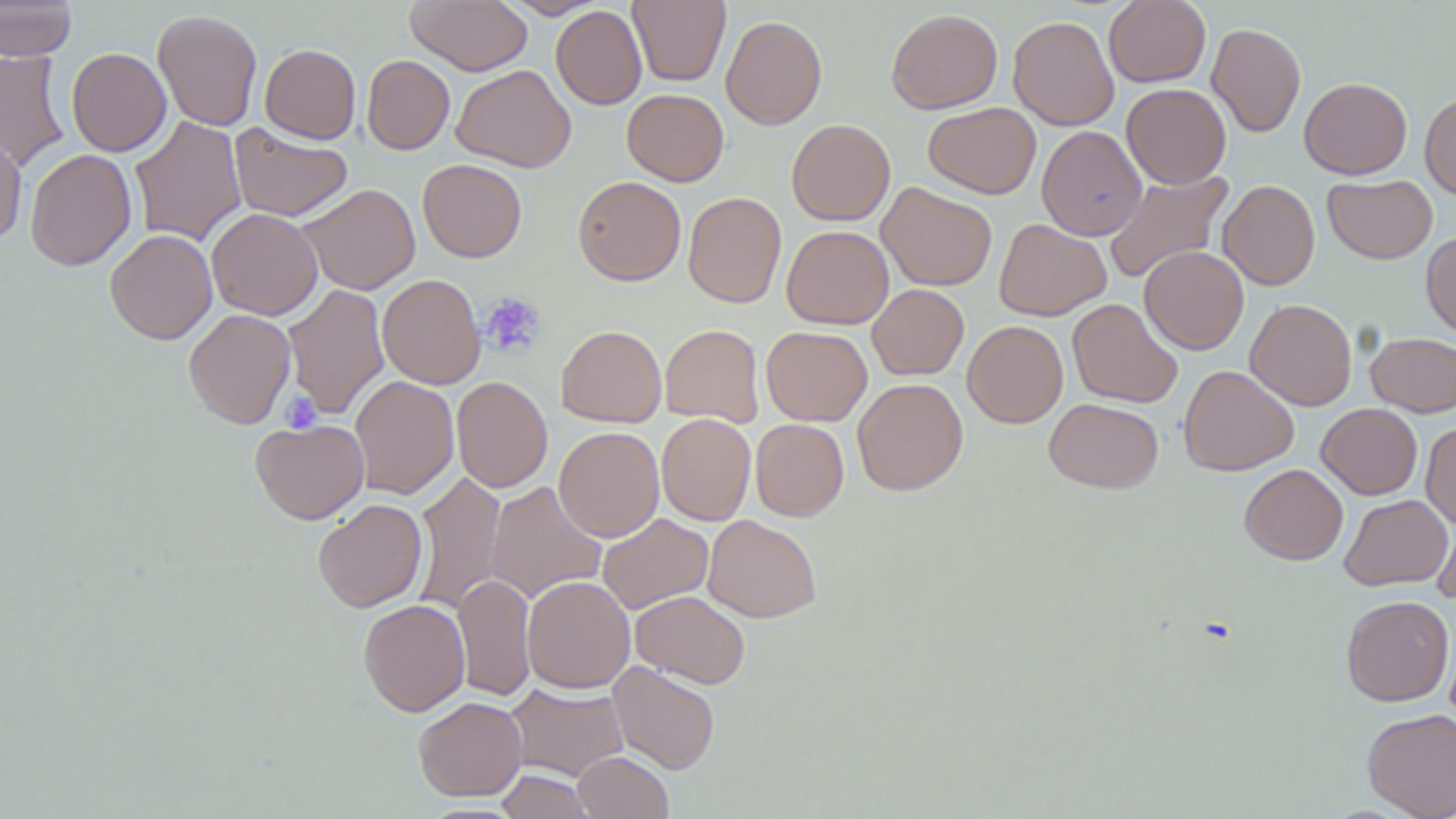
Summary:
  - Coordinate format: approximate bounding boxes as (x1, y1, x2, y2) in pixels
  - Platelet locations: (480, 292, 546, 357), (280, 391, 322, 432)
  - Uninfected red blood cell locations: (0, 0, 78, 61), (406, 0, 533, 75), (500, 0, 607, 19), (628, 0, 730, 86), (1104, 0, 1211, 87), (551, 6, 647, 110), (886, 8, 1003, 114), (152, 9, 263, 131), (721, 14, 827, 130), (1008, 15, 1119, 131), (1207, 23, 1306, 137), (260, 43, 361, 143), (66, 48, 171, 156), (0, 49, 69, 172), (362, 55, 455, 154), (451, 64, 576, 172), (1299, 77, 1412, 179), (1121, 83, 1231, 189), (622, 88, 729, 186), (1419, 92, 1456, 199), (923, 102, 1041, 199), (129, 116, 248, 247), (787, 119, 895, 225), (229, 124, 353, 222), (1036, 125, 1147, 241), (0, 132, 27, 247), (25, 149, 137, 271), (418, 158, 527, 262), (1102, 170, 1234, 286), (1322, 174, 1437, 264), (573, 176, 686, 286), (1218, 180, 1320, 290), (877, 182, 997, 291), (298, 183, 420, 295), (683, 191, 786, 308), (207, 208, 322, 320), (994, 218, 1111, 321), (781, 225, 894, 329), (105, 229, 217, 344), (1421, 231, 1456, 341), (1139, 246, 1249, 355), (377, 274, 485, 389), (283, 283, 390, 420), (867, 284, 969, 380), (1067, 298, 1183, 408), (1245, 298, 1357, 410), (184, 308, 296, 428), (962, 320, 1068, 428), (556, 324, 667, 427), (660, 324, 764, 428), (761, 326, 872, 426), (1365, 332, 1456, 416), (1178, 365, 1299, 476), (350, 375, 459, 500), (452, 376, 552, 492), (852, 378, 968, 495), (1044, 397, 1163, 493), (1317, 403, 1422, 500), (657, 413, 755, 525), (751, 418, 849, 521), (251, 419, 369, 524), (1420, 422, 1456, 529), (554, 426, 664, 542), (1239, 463, 1348, 565), (412, 470, 507, 614), (484, 481, 606, 603), (1339, 494, 1452, 591), (313, 498, 428, 612), (1432, 508, 1456, 603), (597, 513, 713, 614), (702, 515, 821, 622), (453, 574, 536, 703), (522, 575, 635, 693), (630, 591, 750, 688), (1341, 595, 1454, 706), (358, 599, 470, 716), (608, 660, 720, 775), (504, 682, 629, 781), (413, 696, 527, 801), (1362, 708, 1456, 818), (573, 751, 673, 819), (495, 770, 595, 818)
  - Slide-level diagnosis: negative for blood parasites
  - Magnification: 1000x
  - Stain: May-Grünwald-Giemsa
  - Field of view: single
  - Preparation: thin blood smear
  - Image size: 1456×819 pixels
  - Modality: light microscopy